Report the malaria status of this cell.
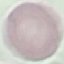
Uninfected.

Automatically extracted cell patch, resized to 64 × 64 pixels. Thin smear of blood. Photographed with a smartphone camera at the microscope eyepiece. Giemsa-stained preparation.